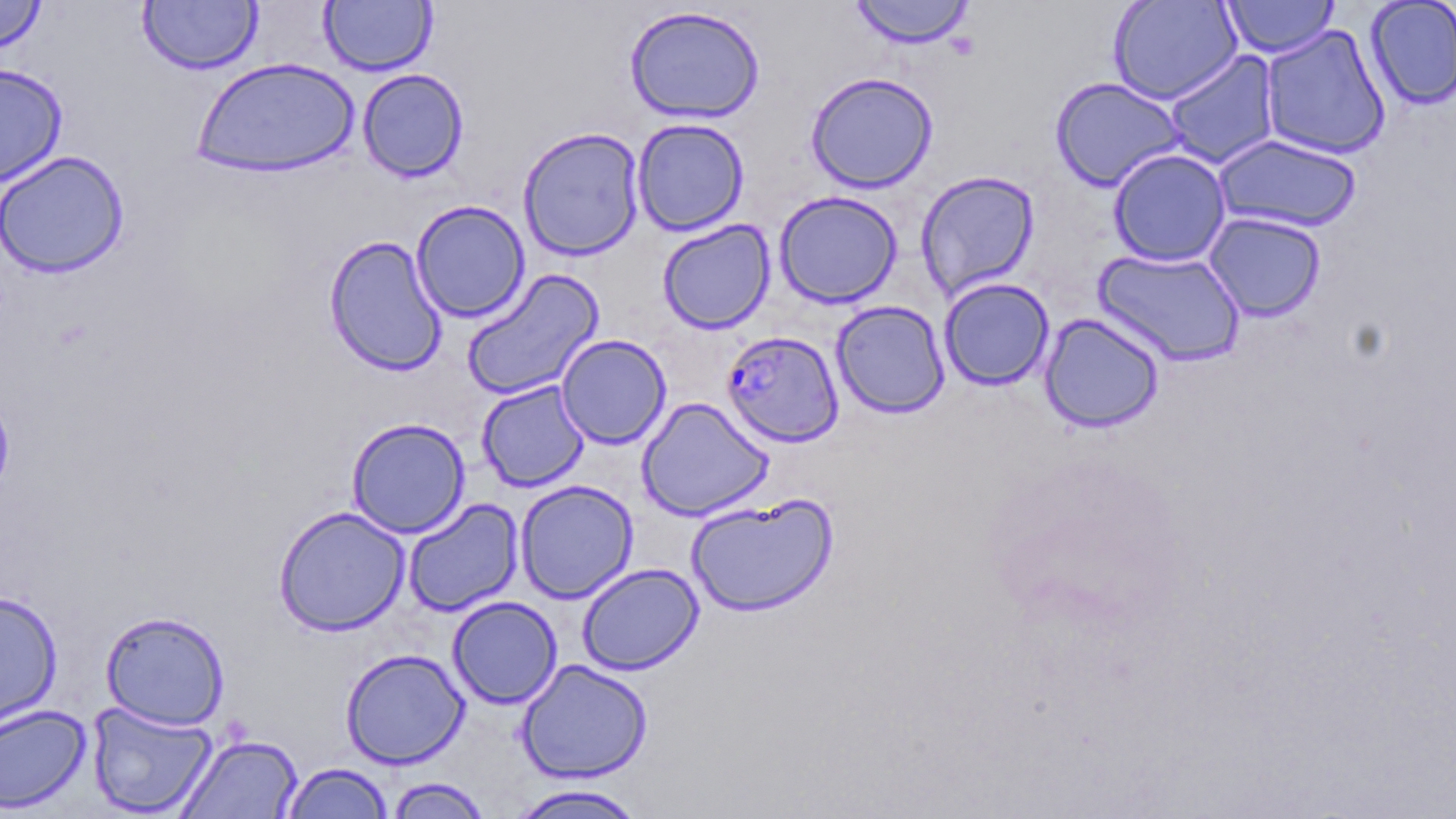

Approximate bounding boxes as named x1/y1/x2/y2 corners in pixels. Uninfected red blood cell locations: (x1=0, y1=0, x2=47, y2=56), (x1=849, y1=0, x2=975, y2=48), (x1=1107, y1=0, x2=1243, y2=105), (x1=1220, y1=0, x2=1340, y2=58), (x1=1364, y1=0, x2=1456, y2=110), (x1=138, y1=1, x2=262, y2=74), (x1=319, y1=1, x2=436, y2=76), (x1=624, y1=5, x2=765, y2=124), (x1=1260, y1=24, x2=1391, y2=160), (x1=1164, y1=50, x2=1281, y2=169), (x1=192, y1=57, x2=360, y2=178), (x1=0, y1=62, x2=68, y2=188), (x1=357, y1=68, x2=469, y2=182), (x1=805, y1=71, x2=938, y2=193), (x1=1050, y1=76, x2=1187, y2=192), (x1=632, y1=118, x2=749, y2=236), (x1=518, y1=126, x2=645, y2=261), (x1=1213, y1=134, x2=1362, y2=233), (x1=1108, y1=148, x2=1231, y2=267), (x1=0, y1=150, x2=130, y2=279), (x1=915, y1=170, x2=1039, y2=299), (x1=774, y1=191, x2=902, y2=308), (x1=410, y1=200, x2=530, y2=323), (x1=1203, y1=212, x2=1326, y2=322), (x1=657, y1=219, x2=776, y2=334), (x1=323, y1=234, x2=448, y2=377), (x1=1093, y1=248, x2=1245, y2=366), (x1=461, y1=268, x2=604, y2=401), (x1=939, y1=277, x2=1055, y2=391), (x1=831, y1=300, x2=950, y2=419), (x1=1039, y1=312, x2=1165, y2=433), (x1=556, y1=334, x2=671, y2=449), (x1=476, y1=380, x2=590, y2=492), (x1=637, y1=397, x2=774, y2=521), (x1=347, y1=417, x2=470, y2=538), (x1=515, y1=480, x2=638, y2=603), (x1=685, y1=494, x2=838, y2=617), (x1=403, y1=498, x2=524, y2=617), (x1=273, y1=505, x2=410, y2=636), (x1=577, y1=563, x2=703, y2=675), (x1=0, y1=588, x2=62, y2=733), (x1=447, y1=596, x2=562, y2=709), (x1=101, y1=610, x2=230, y2=730), (x1=340, y1=648, x2=469, y2=769), (x1=516, y1=658, x2=653, y2=783), (x1=87, y1=701, x2=218, y2=817), (x1=0, y1=703, x2=92, y2=814), (x1=177, y1=733, x2=303, y2=819), (x1=281, y1=762, x2=394, y2=818), (x1=384, y1=776, x2=493, y2=818), (x1=506, y1=784, x2=650, y2=818). Plasmodium falciparum-infected red blood cell locations: (x1=722, y1=330, x2=848, y2=447). Slide-level diagnosis: Plasmodium falciparum. Single field of view. May-Grünwald-Giemsa-stained preparation. Image is 1456×819 pixels. Optical microscopy. Thin blood film. 1000x magnification.